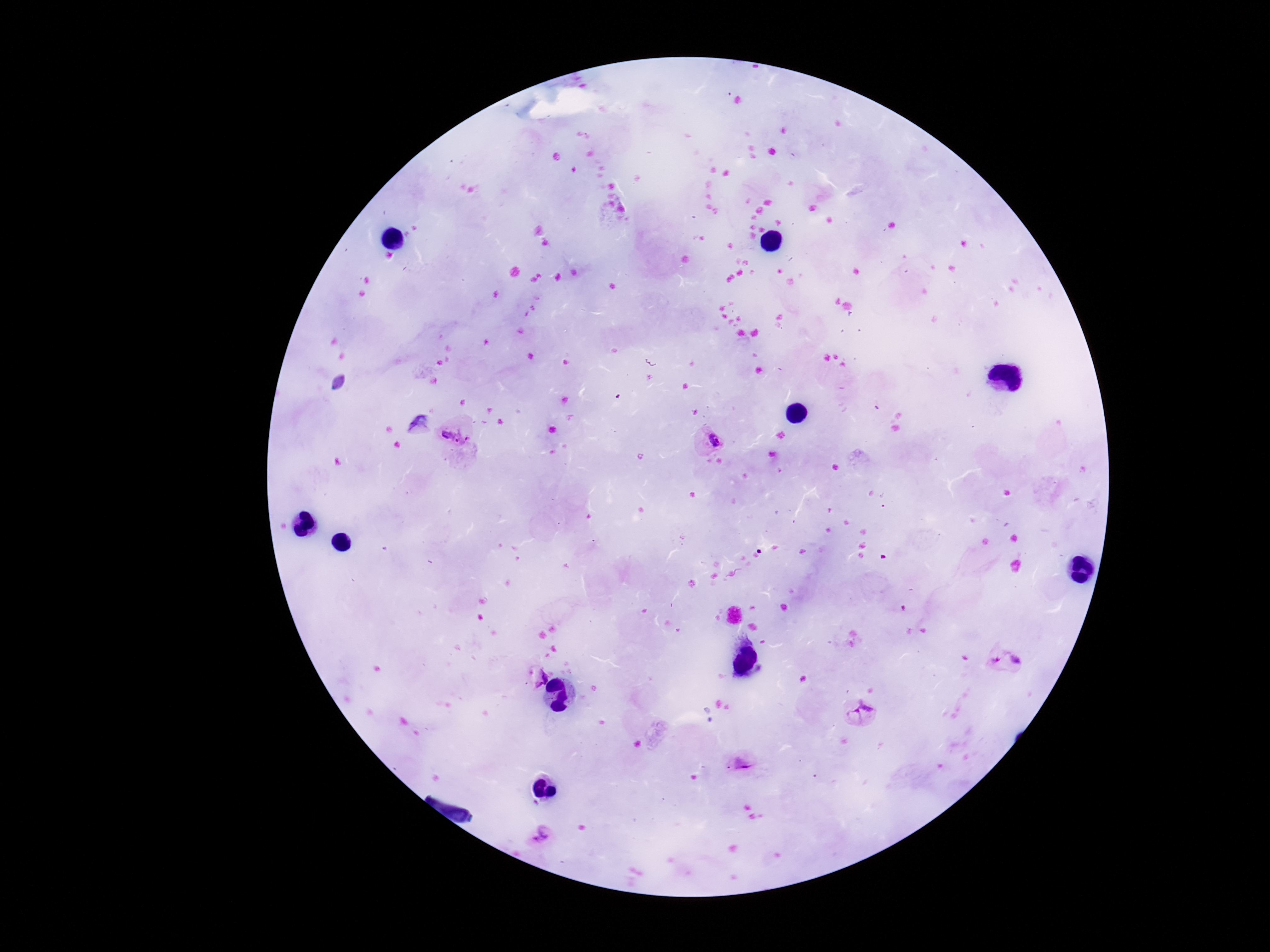
Approximate centers as {x, y} in pixels.
Summary:
  - Plasmodium parasite locations: {418, 426}, {457, 437}, {709, 438}, {1004, 661}, {536, 677}, {861, 713}, {743, 765}, {539, 835}
  - Field of view: single
  - Stain: Giemsa
  - Magnification: 100x
  - Patient malaria status: infected
  - Image size: 1270×952 pixels
  - Capture: smartphone camera through the microscope eyepiece
  - Preparation: thick blood film